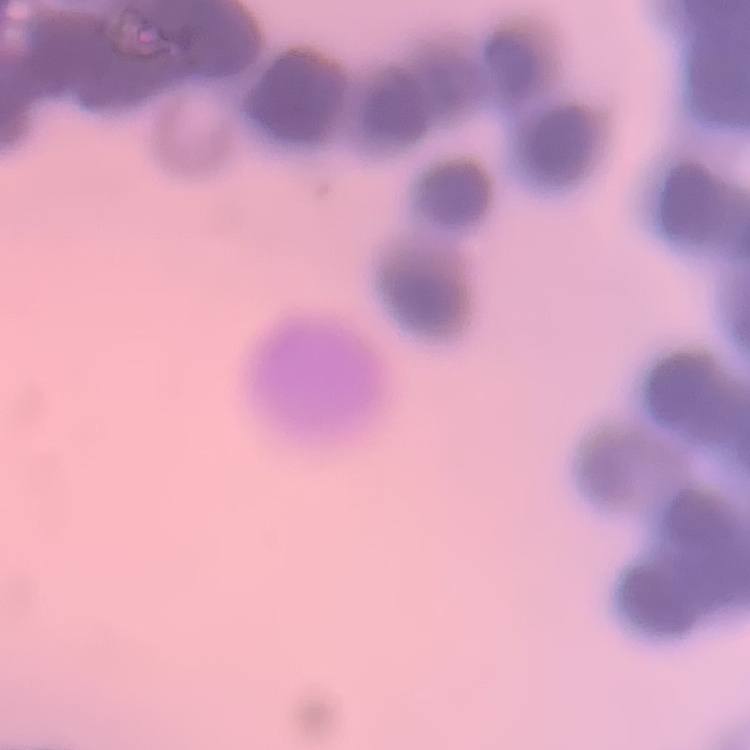
The red blood cells show rouleaux formation. One tile cut from a larger photomicrograph. Thin blood film. Stained with either Field's or Giemsa.